Assess this cell for malaria.
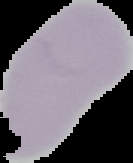

Uninfected.

Summary:
  - Image size: 133×163 pixels
  - Preparation: thin blood film
  - Image type: segmented cell region on a black background